Give the position of every leukocyte visible.
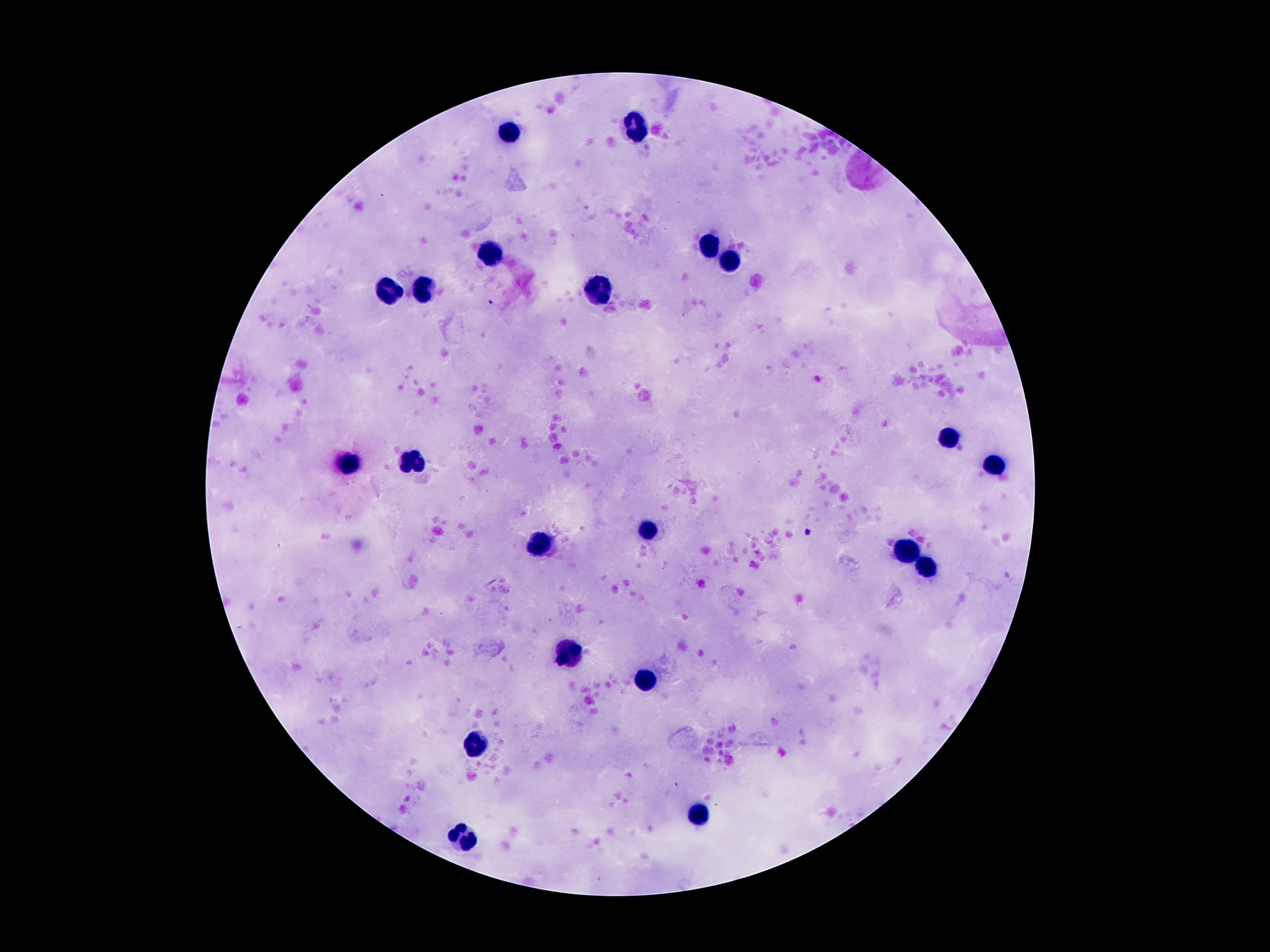

Approximate centers as {x, y} in pixels.
Leukocytes: {632, 126}, {508, 134}, {712, 244}, {489, 249}, {729, 262}, {429, 291}, {391, 292}, {599, 293}, {945, 437}, {414, 461}, {347, 464}, {996, 467}, {651, 530}, {540, 546}, {905, 554}, {928, 567}, {567, 654}, {647, 684}, {479, 748}, {697, 817}, {462, 841}.

image_size: 1270×952 pixels
preparation: thick blood film
patient_malaria_status: uninfected
capture: smartphone camera through the microscope eyepiece
stain: Giemsa
field_of_view: one from this slide
magnification: 100x